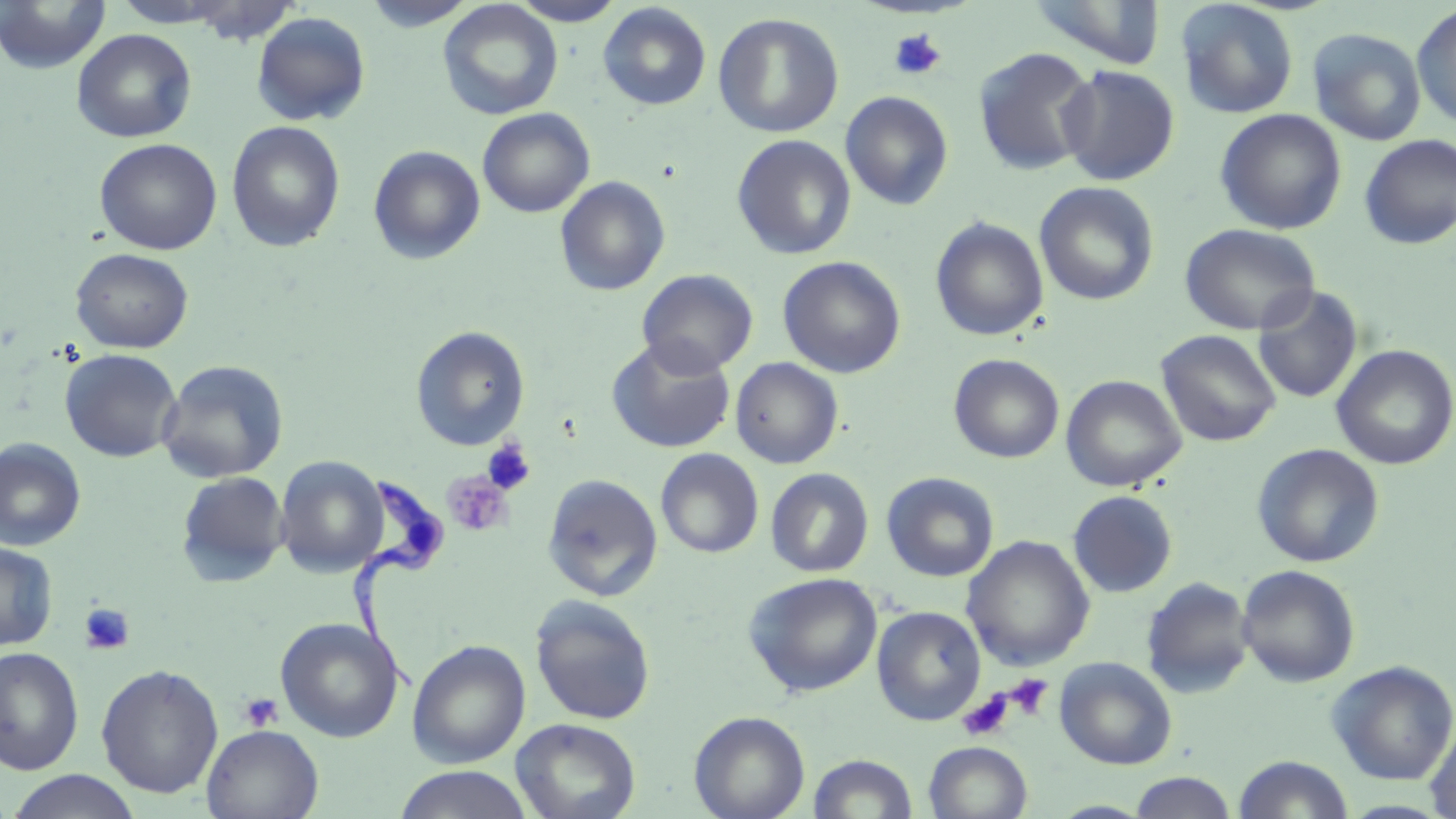

Summary:
  - Coordinate format: approximate bounding boxes as named x1/y1/x2/y2 corners in pixels
  - Platelet locations: (x1=888, y1=28, x2=948, y2=82), (x1=482, y1=439, x2=536, y2=496), (x1=443, y1=471, x2=514, y2=537), (x1=78, y1=603, x2=135, y2=655), (x1=1003, y1=675, x2=1053, y2=720), (x1=957, y1=690, x2=1015, y2=741), (x1=239, y1=693, x2=284, y2=732)
  - Uninfected red blood cell locations: (x1=0, y1=0, x2=111, y2=74), (x1=361, y1=0, x2=478, y2=32), (x1=507, y1=0, x2=627, y2=26), (x1=1025, y1=0, x2=1166, y2=69), (x1=1175, y1=0, x2=1299, y2=119), (x1=437, y1=1, x2=563, y2=121), (x1=598, y1=2, x2=712, y2=111), (x1=1411, y1=3, x2=1456, y2=130), (x1=251, y1=12, x2=371, y2=126), (x1=713, y1=13, x2=844, y2=138), (x1=1307, y1=27, x2=1427, y2=146), (x1=71, y1=28, x2=197, y2=143), (x1=972, y1=47, x2=1099, y2=176), (x1=1057, y1=64, x2=1180, y2=186), (x1=840, y1=91, x2=954, y2=210), (x1=477, y1=108, x2=595, y2=218), (x1=1214, y1=108, x2=1347, y2=234), (x1=225, y1=121, x2=346, y2=252), (x1=732, y1=134, x2=856, y2=260), (x1=1359, y1=135, x2=1456, y2=250), (x1=95, y1=138, x2=222, y2=255), (x1=368, y1=145, x2=486, y2=265), (x1=554, y1=176, x2=670, y2=296), (x1=1034, y1=181, x2=1159, y2=306), (x1=930, y1=216, x2=1049, y2=341), (x1=1179, y1=223, x2=1321, y2=335), (x1=71, y1=248, x2=193, y2=354), (x1=777, y1=255, x2=906, y2=378), (x1=636, y1=268, x2=759, y2=377), (x1=1253, y1=286, x2=1363, y2=404), (x1=414, y1=326, x2=533, y2=451), (x1=1156, y1=329, x2=1281, y2=447), (x1=606, y1=337, x2=736, y2=453), (x1=1331, y1=344, x2=1456, y2=470), (x1=59, y1=349, x2=182, y2=462), (x1=948, y1=353, x2=1064, y2=463), (x1=730, y1=357, x2=843, y2=469), (x1=156, y1=359, x2=289, y2=483), (x1=1061, y1=374, x2=1187, y2=492), (x1=0, y1=438, x2=86, y2=551), (x1=1252, y1=443, x2=1385, y2=568), (x1=655, y1=448, x2=764, y2=558), (x1=275, y1=455, x2=388, y2=577), (x1=765, y1=467, x2=874, y2=578), (x1=176, y1=471, x2=289, y2=586), (x1=881, y1=471, x2=999, y2=582), (x1=542, y1=473, x2=664, y2=602), (x1=1068, y1=490, x2=1177, y2=597), (x1=962, y1=536, x2=1094, y2=671), (x1=0, y1=541, x2=58, y2=651), (x1=1237, y1=565, x2=1360, y2=688), (x1=743, y1=572, x2=883, y2=697), (x1=1141, y1=577, x2=1255, y2=699), (x1=529, y1=595, x2=656, y2=726), (x1=872, y1=606, x2=986, y2=725), (x1=275, y1=617, x2=404, y2=742), (x1=407, y1=639, x2=530, y2=768), (x1=0, y1=646, x2=84, y2=775), (x1=1054, y1=657, x2=1178, y2=770), (x1=1327, y1=660, x2=1456, y2=784), (x1=96, y1=664, x2=223, y2=798), (x1=690, y1=710, x2=810, y2=819), (x1=511, y1=717, x2=640, y2=819), (x1=1425, y1=719, x2=1456, y2=819), (x1=202, y1=724, x2=323, y2=819), (x1=924, y1=741, x2=1033, y2=819), (x1=808, y1=753, x2=918, y2=818), (x1=1232, y1=755, x2=1354, y2=818), (x1=393, y1=766, x2=535, y2=819), (x1=5, y1=770, x2=144, y2=819), (x1=1128, y1=772, x2=1237, y2=818), (x1=1046, y1=800, x2=1155, y2=818)
  - Trypanosoma brucei locations: (x1=348, y1=470, x2=449, y2=699)
  - Slide-level diagnosis: Trypanosoma brucei
  - Stain: May-Grünwald-Giemsa
  - Image size: 1456×819 pixels
  - Magnification: 1000x
  - Preparation: thin blood film
  - Modality: optical microscopy
  - Field of view: single